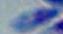

magnification = 1000x
identification = Toxoplasma gondii
modality = photomicrograph